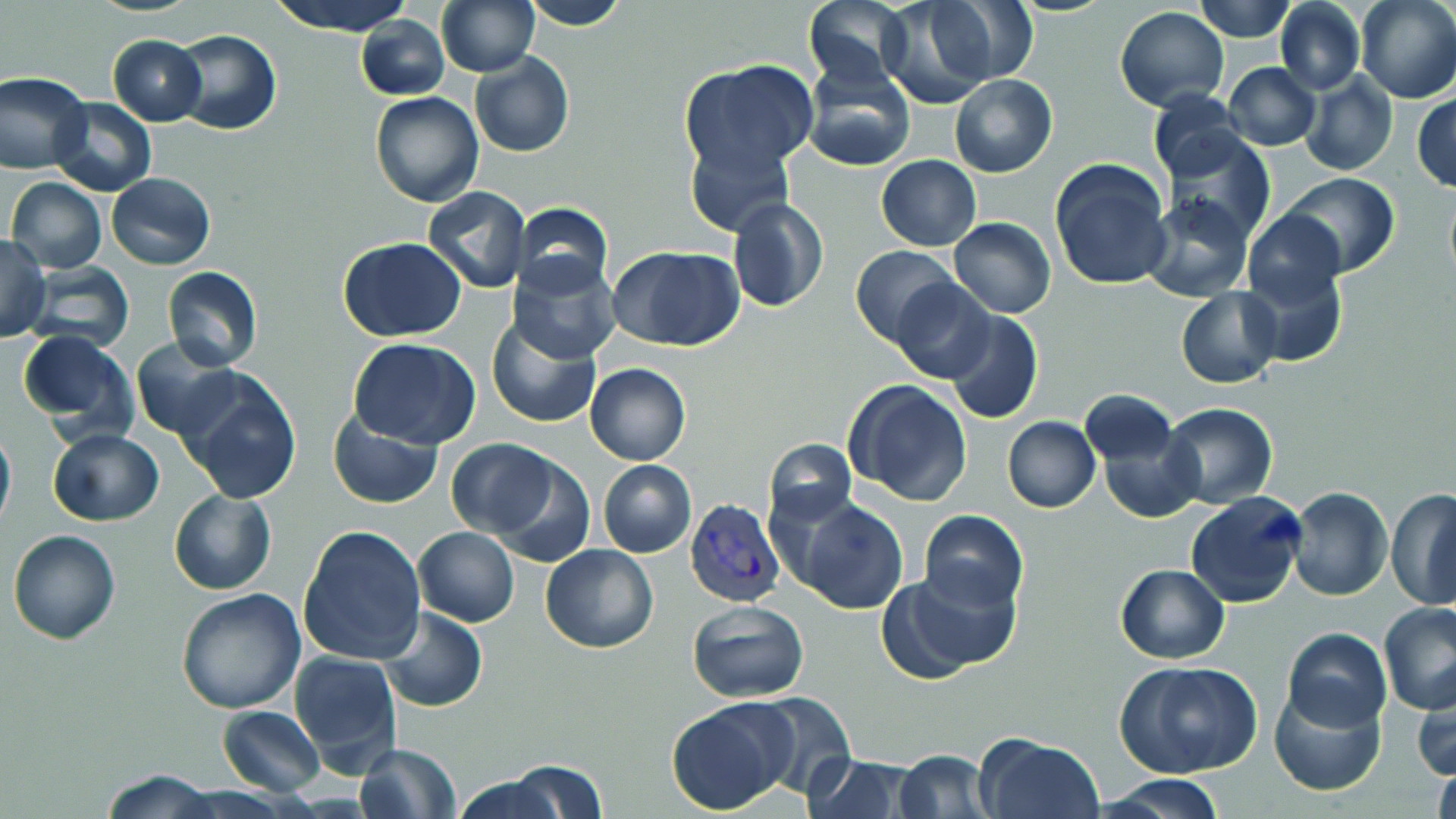

Approximate bounding boxes as (x1,y1)-(x2,y2) corner pairs in pixels. Plasmodium vivax-infected red blood cell locations: (685,501)-(786,608). Uninfected red blood cell locations: (268,0)-(417,37), (435,0)-(539,78), (521,0)-(632,30), (803,0)-(912,92), (877,0)-(1000,110), (926,0)-(1038,92), (1193,0)-(1297,42), (1274,0)-(1366,95), (1355,0)-(1456,103), (1114,6)-(1229,110), (356,14)-(450,102), (171,29)-(282,135), (108,35)-(206,125), (470,51)-(575,159), (681,60)-(818,178), (1224,62)-(1321,151), (800,63)-(916,172), (0,70)-(92,173), (1299,72)-(1398,177), (949,73)-(1059,178), (1148,89)-(1249,181), (369,91)-(484,208), (1412,91)-(1456,192), (49,97)-(156,197), (1160,125)-(1276,243), (684,137)-(793,238), (876,154)-(981,251), (1048,159)-(1174,291), (1278,171)-(1400,276), (107,173)-(215,269), (7,178)-(106,273), (423,186)-(530,294), (1141,195)-(1254,302), (727,197)-(830,313), (513,201)-(613,295), (1243,209)-(1349,309), (948,218)-(1056,317), (0,235)-(50,341), (337,237)-(468,343), (607,245)-(746,351), (850,245)-(958,346), (506,254)-(621,364), (1241,259)-(1347,369), (23,262)-(135,350), (163,267)-(264,370), (890,277)-(996,384), (1176,288)-(1282,388), (944,310)-(1043,425), (485,313)-(604,429), (16,328)-(139,439), (130,337)-(243,440), (349,338)-(480,449), (584,363)-(691,465), (176,370)-(303,503), (843,378)-(974,506), (1080,391)-(1178,468), (1161,403)-(1280,509), (328,412)-(444,511), (1003,416)-(1100,512), (1096,417)-(1203,522), (0,423)-(15,534), (46,428)-(164,527), (446,438)-(564,538), (765,439)-(855,528), (483,454)-(596,568), (598,460)-(696,557), (1386,485)-(1456,610), (1286,486)-(1393,601), (169,488)-(275,595), (1185,492)-(1310,608), (785,495)-(909,614), (919,509)-(1028,613), (297,525)-(427,667), (413,527)-(521,627), (7,529)-(120,645), (540,543)-(659,652), (1116,565)-(1229,662), (893,566)-(1022,675), (175,588)-(307,714), (687,601)-(811,703), (1378,601)-(1456,715), (377,605)-(486,714), (1282,627)-(1391,732), (289,651)-(402,772), (1117,661)-(1264,779), (1413,679)-(1456,785), (1269,682)-(1385,796), (743,691)-(857,797), (665,701)-(793,815), (218,706)-(325,795), (972,732)-(1103,818), (356,743)-(461,819), (893,750)-(995,817), (803,753)-(918,819), (506,759)-(610,818), (1431,759)-(1456,819), (101,769)-(222,818), (1101,773)-(1226,817), (452,775)-(565,819). Slide-level diagnosis: Plasmodium vivax. 1000x magnification. Light microscopy. May-Grünwald-Giemsa-stained preparation. Thin blood film. Single field of view. Image is 1456×819 pixels.